Assess the morphology of the red blood cells.
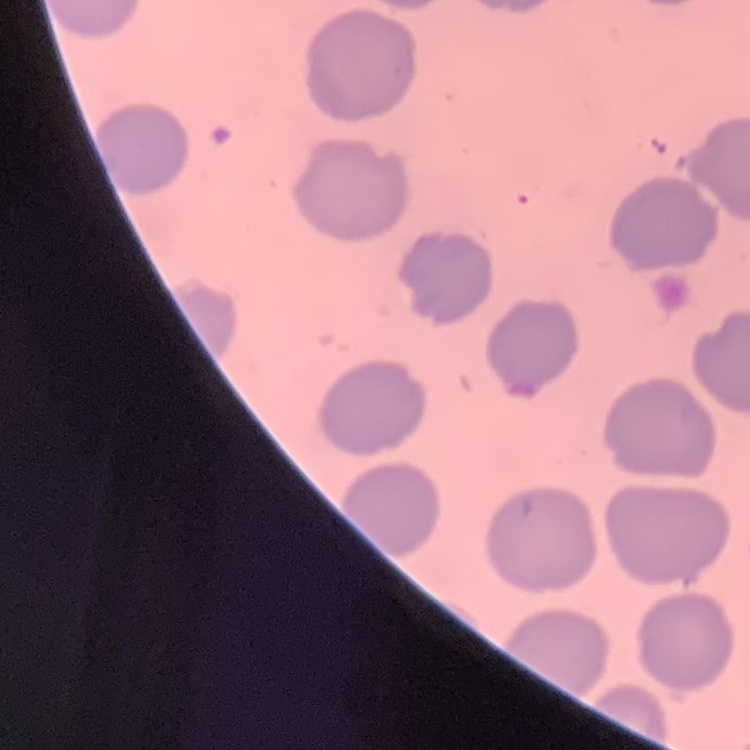
They show no rouleaux formation.

Summary:
  - Stain: Field's or Giemsa
  - Preparation: thin blood smear
  - Image type: square crop of a larger photomicrograph